Point out each leukocyte.
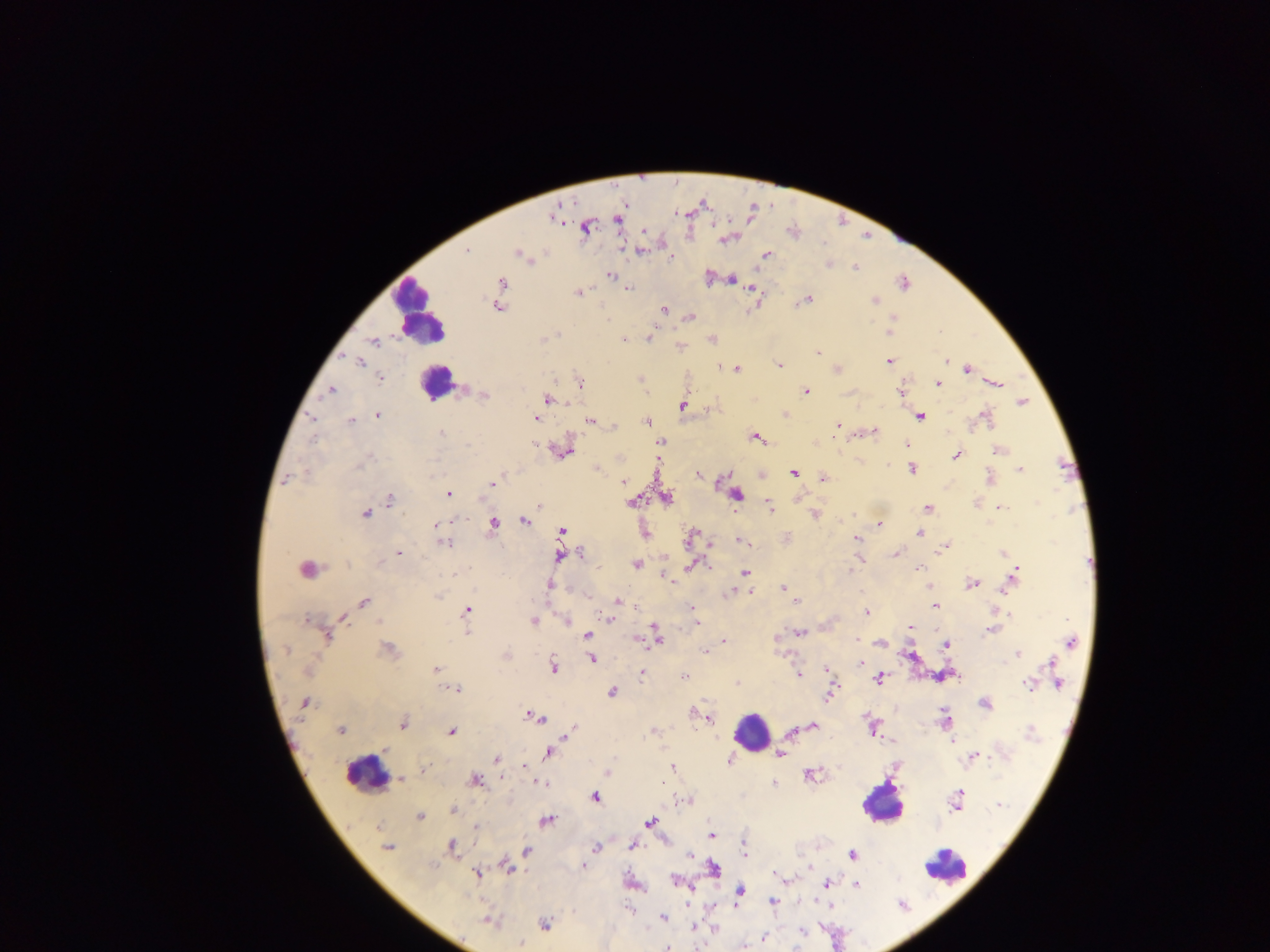
Approximate centers as {x, y} in pixels.
Leukocytes: {418, 312}, {434, 382}, {751, 732}, {366, 773}, {882, 802}, {945, 866}.

preparation = thick blood film
capture = mobile-phone photograph through a microscope
malaria parasite locations = approximate centers as {x, y} in pixels: {554, 217}, {616, 219}, {587, 226}, {727, 239}, {639, 250}, {466, 251}, {519, 253}, {766, 254}, {525, 256}, {670, 258}, {828, 264}, {854, 266}, {610, 275}, {709, 278}, {730, 278}, {903, 281}, {500, 283}, {627, 288}, {753, 289}, {579, 292}, {805, 300}, {874, 300}, {498, 306}, {664, 310}, {689, 317}, {892, 320}, {890, 329}, {648, 338}, {712, 338}, {623, 339}, {373, 341}, {679, 346}, {818, 353}, {947, 360}, {889, 361}, {359, 362}, {779, 365}, {966, 368}, {736, 369}, {836, 369}, {380, 377}, {640, 379}, {938, 383}, {994, 383}, {579, 384}, {331, 390}, {805, 391}, {901, 391}, {483, 395}, {547, 398}, {1022, 402}, {683, 406}, {378, 415}, {785, 415}, {920, 415}, {534, 417}, {984, 417}, {350, 421}, {592, 421}, {646, 422}, {836, 424}, {615, 425}, {873, 430}, {441, 434}, {756, 437}, {661, 441}, {906, 444}, {562, 449}, {999, 450}, {956, 454}, {658, 458}, {597, 468}, {911, 468}, {1019, 469}, {793, 472}, {698, 474}, {761, 474}, {823, 478}, {989, 478}, {287, 479}, {623, 481}, {493, 483}, {448, 493}, {735, 494}, {666, 497}, {796, 498}, {389, 499}, {631, 500}, {976, 503}, {538, 505}, {769, 508}, {927, 508}, {999, 508}, {365, 513}, {814, 514}, {524, 521}, {879, 523}, {493, 524}, {435, 525}, {561, 530}, {644, 533}, {919, 533}, {690, 537}, {857, 538}, {786, 539}, {743, 541}, {442, 542}, {947, 545}, {398, 552}, {581, 552}, {1003, 552}, {895, 553}, {560, 555}, {859, 559}, {636, 564}, {691, 565}, {919, 567}, {307, 568}, {744, 573}, {1013, 575}, {667, 578}, {971, 584}, {549, 586}, {930, 586}, {784, 588}, {749, 591}, {729, 593}, {587, 596}, {617, 601}, {796, 601}, {363, 602}, {934, 605}, {635, 606}, {692, 607}, {466, 609}, {865, 613}, {342, 617}, {610, 619}, {533, 620}, {566, 620}, {695, 623}, {909, 628}, {991, 628}, {465, 631}, {798, 633}, {325, 635}, {656, 635}, {587, 636}, {775, 639}, {723, 641}, {1070, 641}, {880, 643}, {945, 645}, {388, 649}, {704, 651}, {1018, 652}, {505, 655}, {910, 656}, {592, 658}, {1052, 662}, {861, 663}, {553, 666}, {436, 670}, {827, 670}, {642, 672}, {797, 674}, {943, 675}, {683, 677}, {1056, 677}, {878, 678}, {737, 683}, {1029, 684}, {1058, 684}, {456, 688}, {611, 692}, {830, 694}, {305, 703}, {984, 703}, {693, 712}, {532, 715}, {709, 717}, {945, 718}, {402, 722}, {812, 725}, {872, 727}, {340, 729}, {571, 730}, {450, 731}, {654, 731}, {793, 732}, {891, 742}, {951, 742}, {549, 751}, {780, 753}, {972, 757}, {496, 758}, {729, 760}, {525, 766}, {671, 767}, {425, 769}, {607, 773}, {809, 773}, {401, 780}, {475, 780}, {538, 782}, {663, 782}, {773, 782}, {594, 796}, {956, 800}, {683, 801}, {998, 805}, {453, 809}, {420, 816}, {546, 821}, {650, 822}, {476, 827}, {709, 834}, {632, 845}, {452, 846}, {387, 847}, {596, 847}, {745, 849}, {527, 851}, {687, 852}, {851, 854}, {582, 866}, {809, 867}, {508, 868}, {714, 868}, {476, 873}, {785, 879}, {676, 881}, {630, 883}, {856, 883}, {826, 884}, {738, 891}, {772, 902}, {828, 906}, {663, 917}, {488, 920}, {545, 923}, {693, 927}, {714, 929}, {763, 937}, {519, 942}, {667, 946}, {742, 947}
image size = 1270×952 pixels
field of view = single
country = Ghana